Identify the parasite.
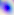

This is Toxoplasma gondii.

Summary:
  - Magnification: 400x
  - Modality: photomicrograph